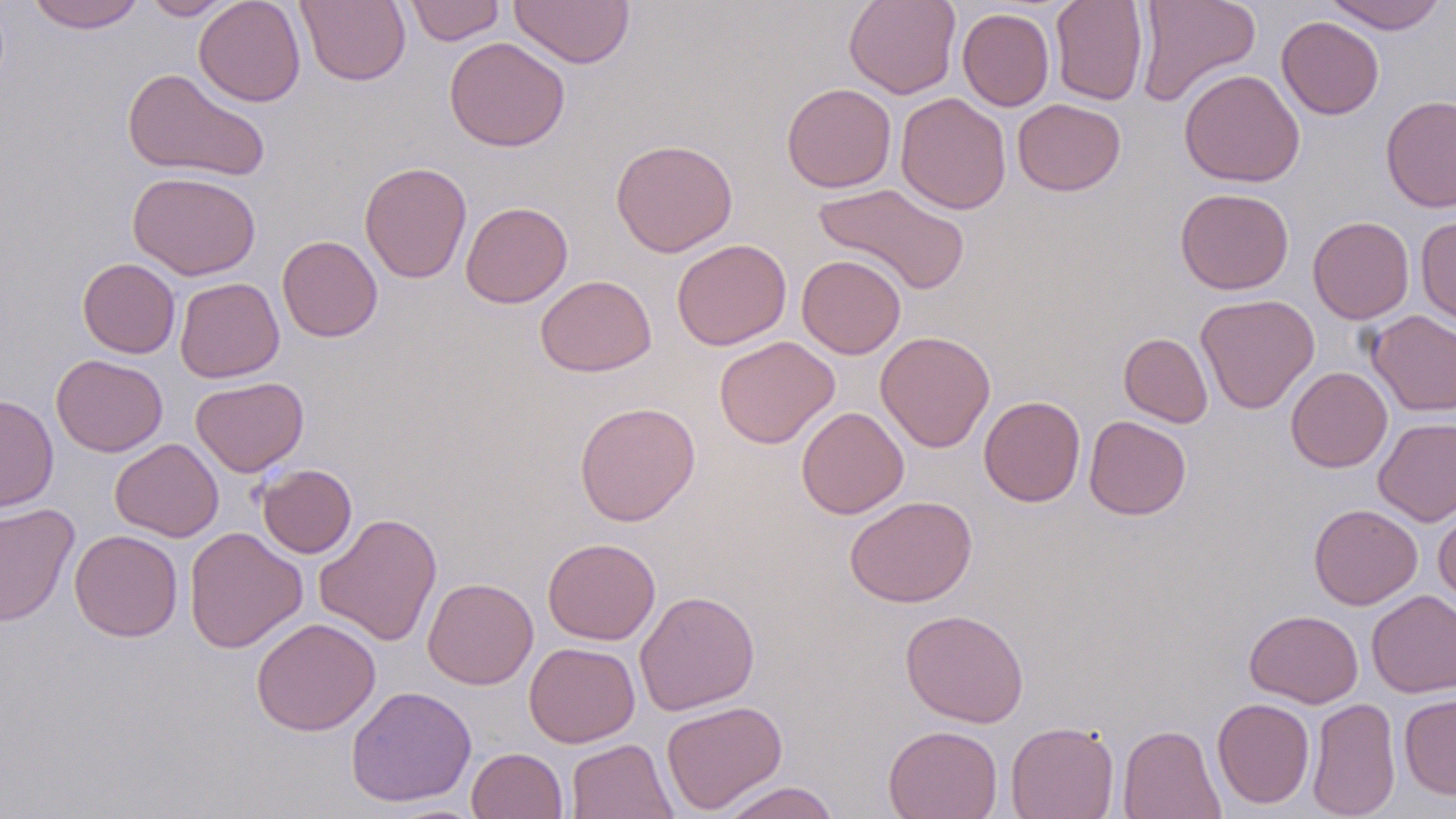

slide_level_diagnosis: no evidence of blood parasites
preparation: thin blood smear
image_size: 1456×819 pixels
modality: optical microscopy
magnification: 1000x
uninfected_red_blood_cell_locations: 'approximate bounding boxes as (x1, y1, x2, y2) in pixels: (27, 0, 145, 33), (141, 0, 237, 20), (193, 0, 306, 107), (296, 0, 411, 87), (403, 0, 506, 45), (508, 0, 635, 68), (843, 0, 961, 99), (1050, 0, 1149, 106), (1134, 0, 1260, 106), (1322, 0, 1448, 34), (957, 8, 1055, 111), (1276, 16, 1384, 120), (444, 36, 570, 152), (122, 68, 270, 181), (1179, 68, 1305, 188), (781, 83, 897, 193), (896, 92, 1011, 215), (1380, 95, 1456, 212), (1012, 99, 1126, 196), (610, 138, 738, 257), (359, 160, 472, 284), (127, 171, 262, 280), (813, 182, 971, 296), (1175, 187, 1294, 294), (460, 201, 574, 308), (1416, 215, 1456, 326), (1308, 216, 1414, 324), (277, 235, 383, 342), (671, 239, 791, 351), (797, 254, 906, 359), (77, 258, 180, 358), (535, 274, 656, 377), (174, 277, 284, 382), (1196, 294, 1319, 414), (1366, 310, 1456, 416), (875, 331, 995, 453), (1119, 333, 1213, 428), (714, 335, 840, 448), (51, 354, 168, 457), (1286, 366, 1392, 472), (190, 376, 309, 477), (0, 394, 58, 512), (979, 395, 1085, 507), (573, 401, 701, 526), (796, 407, 909, 519), (1084, 416, 1191, 520), (1373, 417, 1456, 526), (109, 438, 223, 542), (257, 464, 357, 558), (843, 495, 977, 608), (0, 502, 79, 626), (1308, 503, 1423, 609), (1433, 505, 1456, 609), (314, 512, 442, 646), (184, 526, 307, 654), (69, 529, 183, 642), (542, 537, 660, 644), (422, 577, 539, 689), (634, 590, 760, 715), (1366, 590, 1456, 698), (900, 609, 1029, 727), (1245, 609, 1363, 707), (251, 616, 380, 736), (524, 642, 640, 747), (345, 686, 477, 807), (1398, 694, 1456, 798), (1212, 697, 1315, 809), (1307, 697, 1400, 819), (660, 699, 788, 814), (1006, 720, 1119, 819), (883, 724, 1003, 819), (1118, 724, 1225, 819), (566, 738, 678, 819), (466, 747, 567, 819), (718, 781, 841, 819)'
stain: May-Grünwald-Giemsa
field_of_view: one of a larger specimen